Name the blood parasite species.
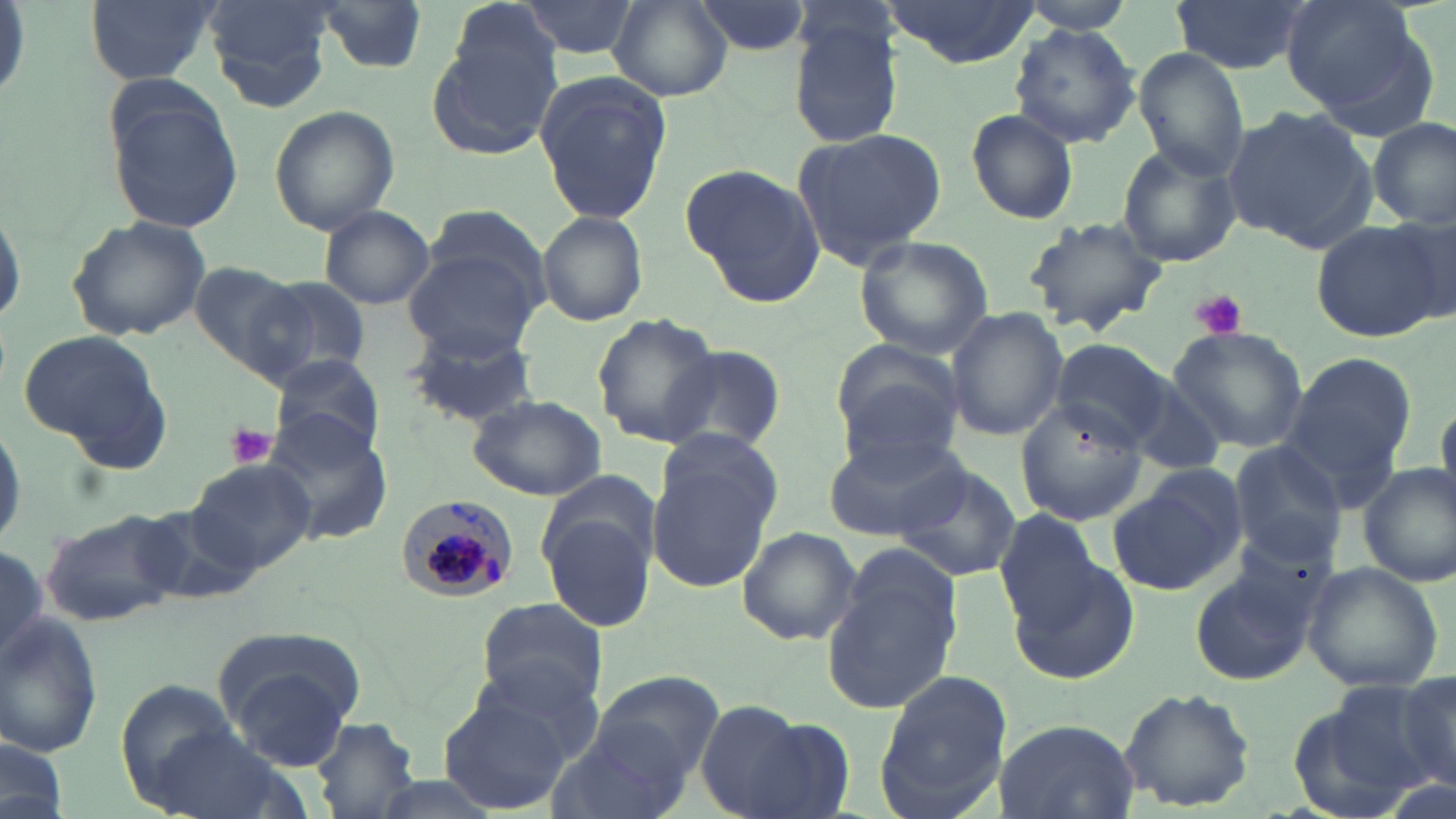
Plasmodium malariae.

Approximate bounding boxes as [x1, y1, x2, y2] in pixels. Platelet locations: [1188, 289, 1247, 340], [227, 423, 278, 471]. Plasmodium malariae-infected red blood cell locations: [397, 493, 521, 603]. Uninfected red blood cell locations: [85, 0, 217, 85], [201, 0, 333, 111], [686, 0, 819, 59], [881, 0, 1041, 67], [1171, 0, 1309, 76], [1278, 0, 1432, 123], [607, 1, 731, 102], [1014, 1, 1137, 34], [310, 2, 430, 74], [446, 2, 564, 109], [513, 2, 640, 59], [786, 8, 906, 150], [1011, 23, 1141, 149], [427, 27, 556, 159], [1136, 48, 1247, 180], [536, 71, 670, 224], [104, 91, 248, 235], [269, 105, 400, 234], [1222, 106, 1377, 251], [963, 108, 1079, 226], [1370, 117, 1455, 230], [789, 125, 949, 270], [1116, 143, 1243, 269], [681, 164, 825, 307], [0, 198, 27, 335], [318, 206, 434, 310], [414, 206, 554, 328], [535, 210, 650, 326], [66, 214, 211, 342], [1020, 214, 1168, 336], [1311, 220, 1446, 342], [853, 235, 993, 359], [401, 251, 540, 361], [185, 259, 308, 372], [247, 276, 372, 386], [946, 308, 1067, 440], [591, 314, 721, 446], [401, 323, 545, 429], [1168, 327, 1309, 453], [15, 330, 175, 471], [1052, 337, 1174, 450], [829, 338, 964, 460], [660, 342, 784, 456], [1278, 351, 1418, 505], [268, 352, 387, 460], [1434, 393, 1456, 518], [466, 395, 605, 500], [1017, 398, 1152, 524], [261, 409, 395, 548], [0, 415, 26, 555], [823, 432, 965, 543], [1227, 441, 1349, 564], [649, 456, 778, 592], [185, 460, 319, 572], [892, 462, 1021, 583], [1357, 466, 1456, 588], [1104, 467, 1246, 595], [538, 470, 660, 574], [136, 504, 263, 610], [537, 506, 656, 633], [39, 507, 187, 627], [994, 508, 1104, 632], [735, 526, 861, 647], [823, 544, 965, 717], [0, 546, 50, 673], [1012, 556, 1138, 687], [1304, 563, 1442, 692], [1190, 573, 1314, 686], [475, 595, 610, 713], [1, 611, 104, 761], [221, 650, 358, 770], [471, 654, 607, 765], [874, 668, 1011, 816], [591, 670, 724, 781], [1393, 672, 1456, 791], [115, 681, 243, 807], [1285, 684, 1447, 815], [1119, 686, 1258, 813], [437, 692, 568, 813], [695, 701, 813, 818], [310, 715, 420, 819], [745, 716, 856, 819], [991, 719, 1140, 818], [550, 721, 691, 819], [145, 726, 280, 819], [0, 741, 66, 818]. Image is 1456×819 pixels. Thin blood smear. Captured at 1000x magnification. Optical microscopy. One field of a larger specimen. May-Grünwald-Giemsa-stained preparation.